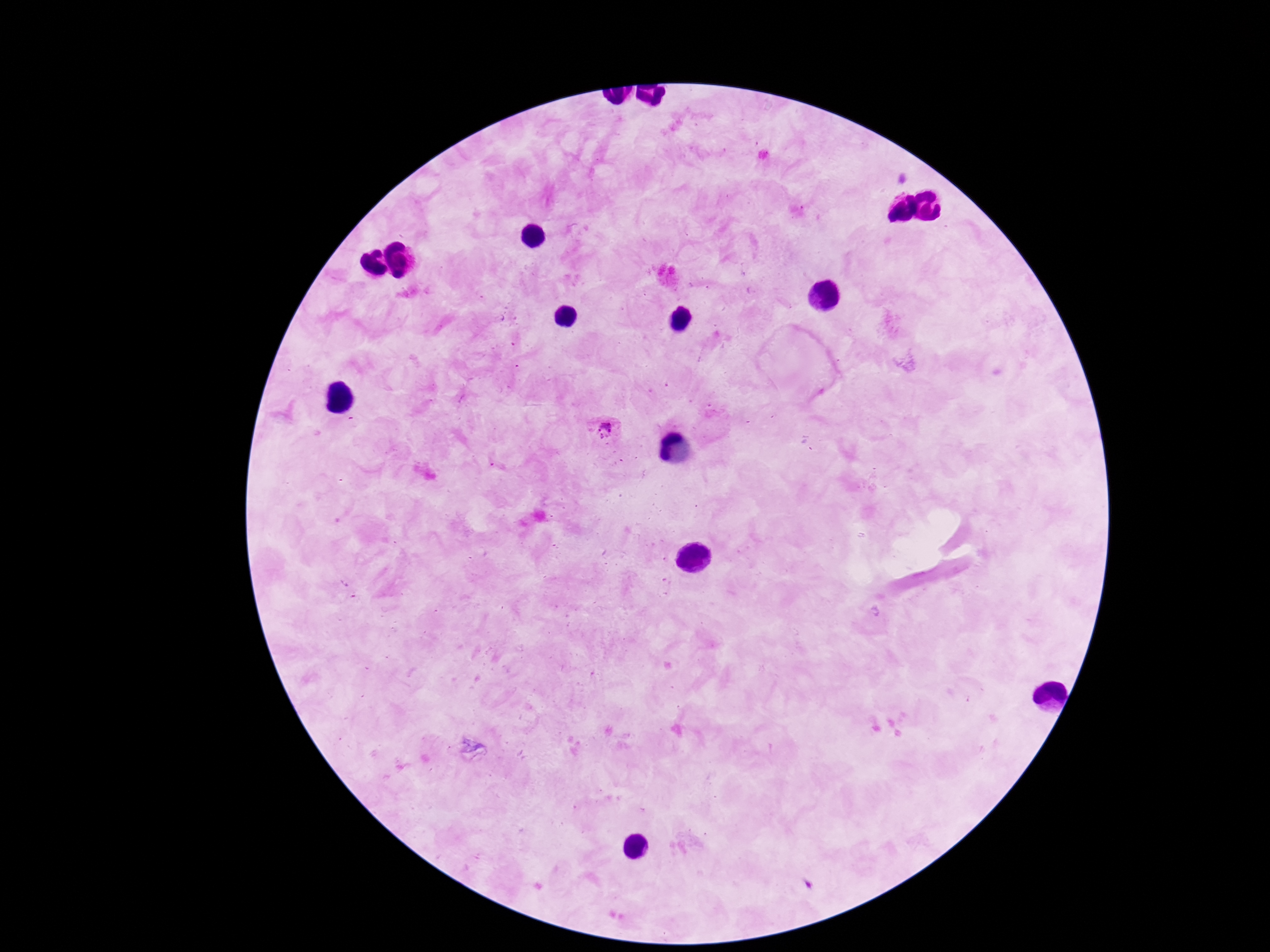
preparation = thick blood smear
magnification = 100x
capture = smartphone camera through the microscope eyepiece
Plasmodium parasite locations = approximate object centers, in pixels from the top-left corner: (x=607, y=430)
patient malaria status = infected
stain = Giemsa
image size = 1270×952 pixels
field of view = one from this slide